Give the position of every Plasmodium parasite visible.
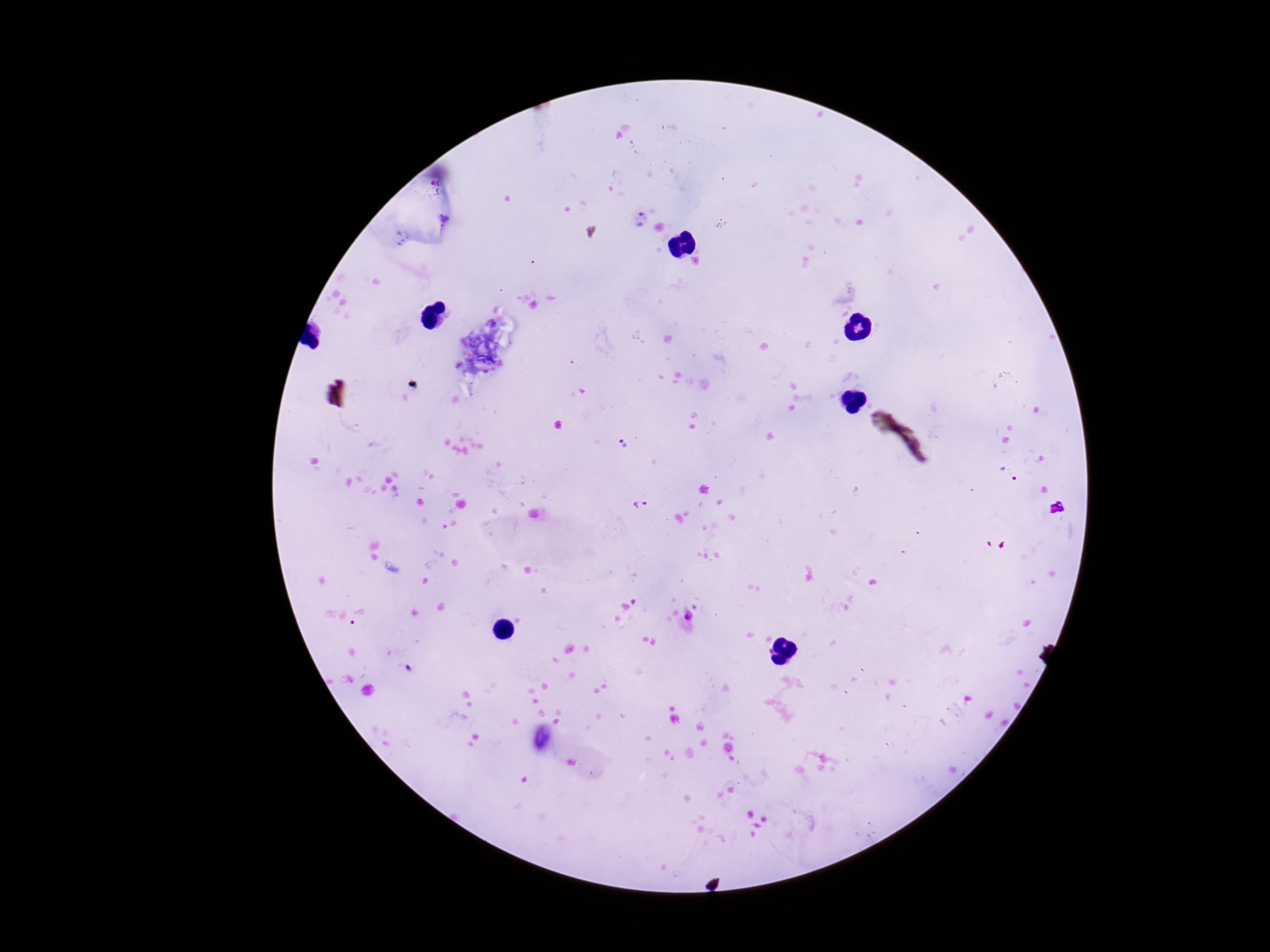

Approximate centers as (x, y) in pixels.
Plasmodium parasites: (638, 218), (623, 443), (1007, 473), (641, 505), (689, 615).

field of view = one from this slide
capture = smartphone camera through the microscope eyepiece
magnification = 100x
patient malaria status = positive
image size = 1270×952 pixels
stain = Giemsa
preparation = thick blood smear